Assess this cell for malaria.
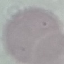
It is uninfected.

Summary:
  - Stain: Giemsa
  - Image type: cell patch, automatically extracted from a larger field of view and resized to 64 × 64 pixels
  - Preparation: thin blood smear
  - Capture: smartphone camera at the microscope eyepiece